Locate every Plasmodium vivax-infected red blood cell.
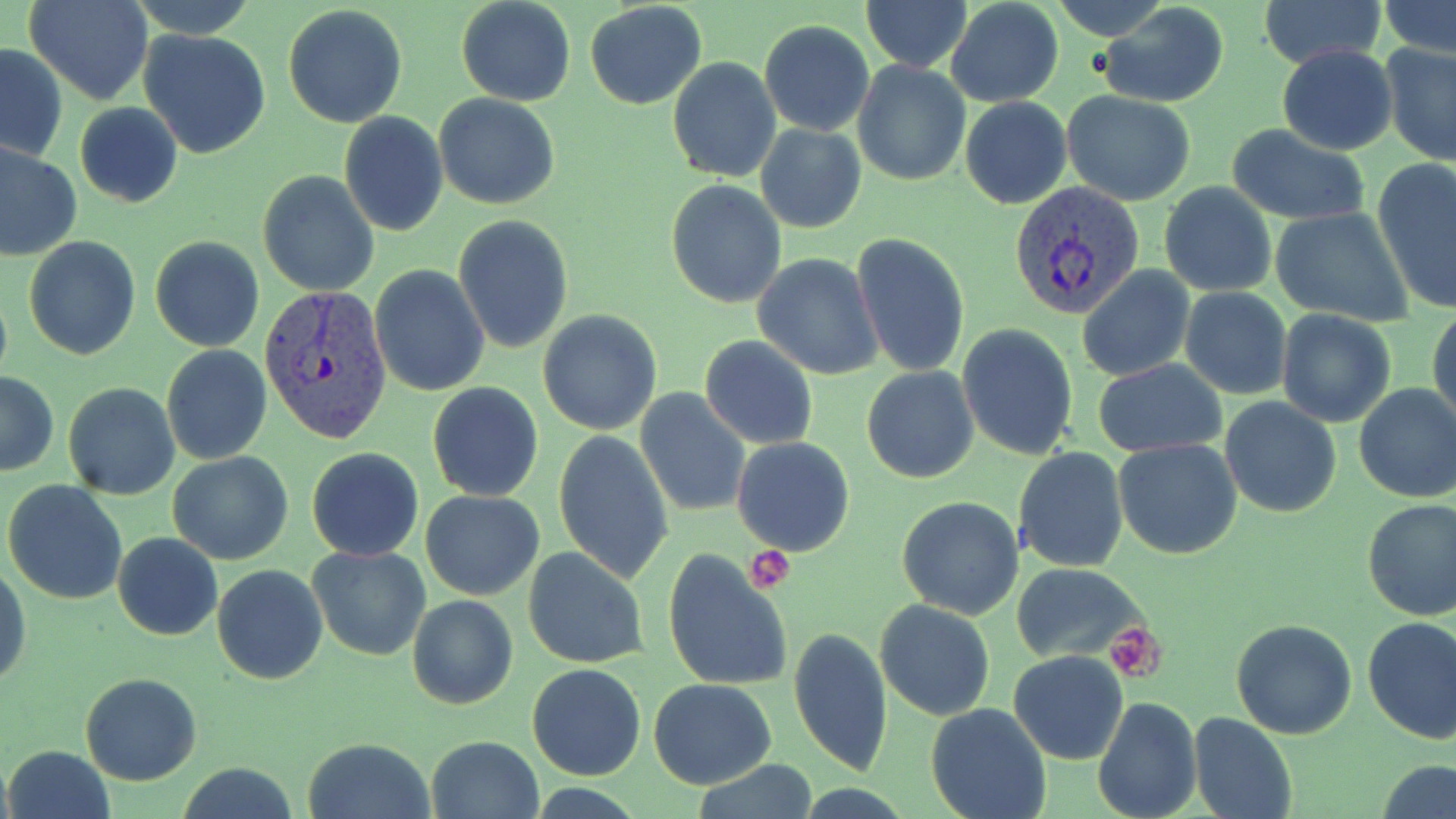

Approximate bounding boxes as (x1,y1)-(x2,y2) corner pairs in pixels.
Plasmodium vivax-infected red blood cells: (1009,181)-(1143,320), (259,284)-(394,445).

slide-level diagnosis = Plasmodium vivax
platelet locations = approximate bounding boxes as (x1,y1)-(x2,y2) corner pairs in pixels: (743,548)-(796,593), (1105,624)-(1166,680)
image size = 1456×819 pixels
stain = May-Grünwald-Giemsa
magnification = 1000x
field of view = one of a larger specimen
uninfected red blood cell locations = approximate bounding boxes as (x1,y1)-(x2,y2) corner pairs in pixels: (25,0)-(152,105), (456,0)-(577,107), (1045,0)-(1175,43), (1258,0)-(1385,68), (1379,0)-(1456,56), (126,1)-(260,38), (585,1)-(707,109), (861,1)-(971,74), (945,1)-(1064,108), (1095,2)-(1232,109), (283,5)-(409,128), (758,20)-(875,136), (139,29)-(272,159), (1380,40)-(1456,164), (1,43)-(69,163), (1276,44)-(1399,155), (666,57)-(781,183), (852,59)-(972,186), (1062,90)-(1196,206), (434,95)-(560,209), (960,97)-(1072,209), (74,103)-(182,207), (338,111)-(449,239), (756,123)-(866,233), (1225,126)-(1372,224), (0,142)-(80,262), (1372,159)-(1456,313), (258,171)-(378,296), (666,179)-(788,308), (1158,181)-(1279,297), (1268,207)-(1414,326), (454,215)-(574,355), (850,233)-(970,380), (150,235)-(265,352), (24,237)-(142,359), (753,252)-(883,380), (369,265)-(490,397), (1077,267)-(1195,382), (1179,288)-(1291,400), (1429,304)-(1456,430), (1275,309)-(1397,427), (537,310)-(662,435), (955,323)-(1080,460), (699,337)-(818,451), (161,343)-(272,465), (1092,359)-(1226,457), (862,366)-(979,483), (0,371)-(59,477), (63,382)-(179,500), (1353,382)-(1456,503), (427,383)-(543,501), (635,387)-(751,518), (1220,396)-(1341,517), (553,430)-(673,585), (732,437)-(855,555), (1115,438)-(1242,558), (306,446)-(423,561), (1012,446)-(1128,573), (168,451)-(293,565), (3,480)-(128,605), (420,489)-(545,600), (896,496)-(1025,620), (1362,500)-(1456,621), (112,532)-(222,641), (306,545)-(433,662), (522,547)-(649,670), (662,548)-(796,692), (0,558)-(30,692), (1009,562)-(1145,661), (211,564)-(327,684), (406,594)-(518,710), (875,600)-(995,720), (1362,616)-(1456,743), (1231,618)-(1360,739), (788,626)-(894,778), (1008,650)-(1128,764), (527,664)-(646,781), (80,672)-(201,785), (648,678)-(776,789), (1092,696)-(1202,819), (926,702)-(1053,819), (1188,710)-(1298,819), (301,736)-(436,819), (425,736)-(544,819), (5,745)-(114,819), (1377,759)-(1456,817), (689,762)-(819,818)
modality = light microscopy
preparation = thin blood smear